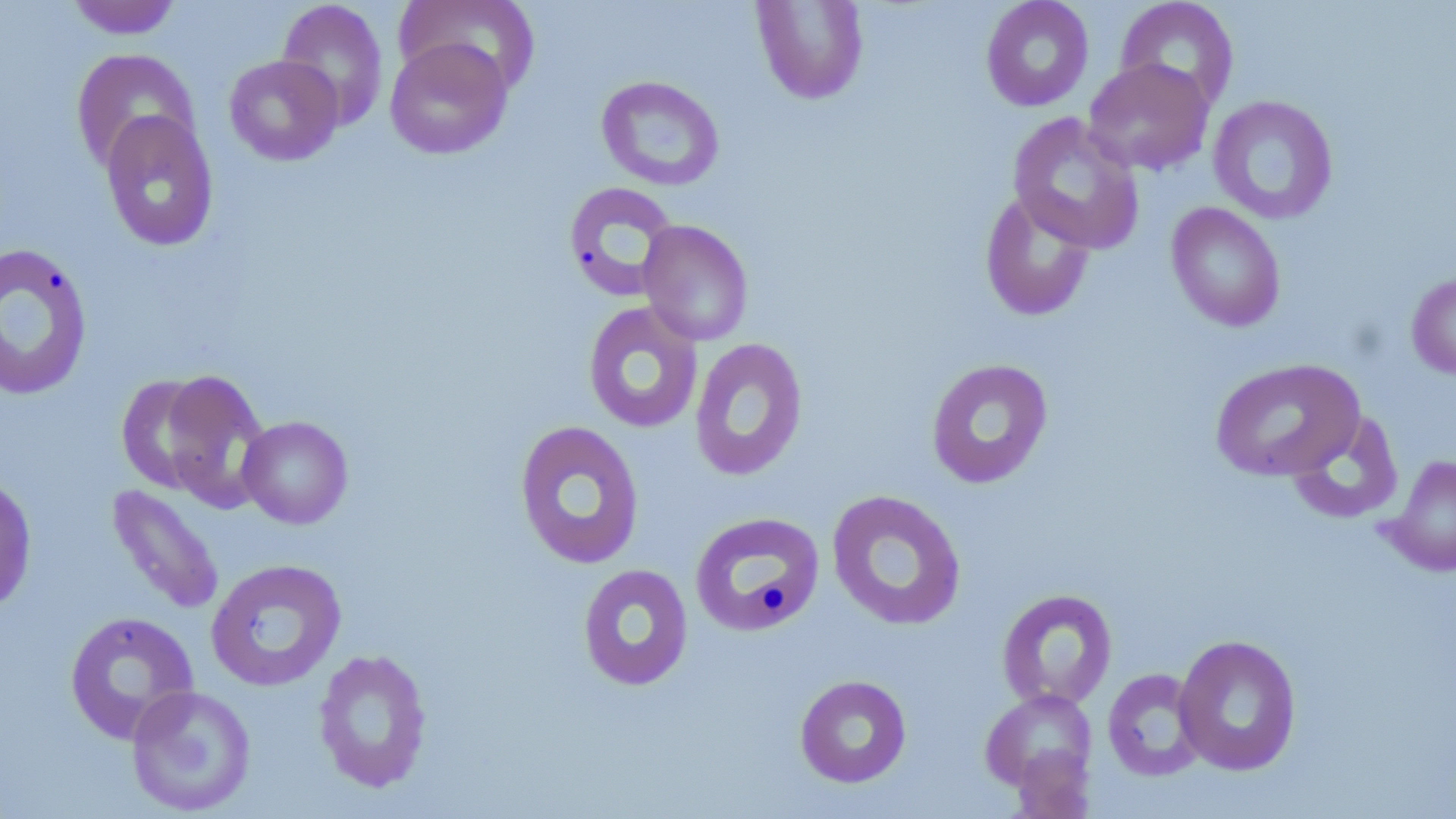 Approximate bounding boxes as [x1, y1, x2, y2] in pixels. Uninfected red blood cell locations: [65, 0, 183, 40], [276, 0, 389, 131], [393, 0, 540, 96], [751, 0, 870, 106], [980, 0, 1094, 112], [1115, 0, 1240, 112], [384, 38, 513, 160], [71, 48, 200, 172], [223, 54, 344, 166], [1083, 58, 1214, 176], [596, 74, 725, 191], [1208, 95, 1339, 225], [100, 110, 220, 252], [1007, 112, 1146, 255], [563, 181, 681, 302], [980, 189, 1096, 322], [1166, 202, 1286, 332], [637, 219, 754, 346], [0, 241, 95, 403], [1407, 270, 1456, 380], [582, 301, 704, 434], [689, 337, 809, 481], [925, 358, 1054, 489], [1209, 358, 1366, 482], [149, 370, 272, 508], [116, 373, 224, 494], [1286, 411, 1404, 526], [237, 415, 354, 529], [513, 419, 646, 570], [1383, 453, 1456, 577], [0, 472, 38, 614], [107, 484, 225, 617], [826, 489, 967, 631], [689, 511, 825, 638], [205, 558, 347, 692], [577, 563, 694, 692], [997, 588, 1118, 711], [64, 611, 200, 744], [1173, 633, 1303, 776], [313, 648, 433, 794], [1103, 667, 1207, 781], [794, 674, 912, 788], [126, 684, 257, 816], [980, 688, 1098, 798]. Slide-level diagnosis: no evidence of blood parasites. May-Grünwald-Giemsa-stained preparation. Light microscopy. Image is 1456×819 pixels. Single field of view. Thin blood film. 1000x magnification.